Report the malaria status of this cell.
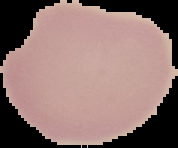
It is uninfected.

preparation: thin blood film
image_size: 178×148 pixels
image_type: segmented cell region with the area outside set to black